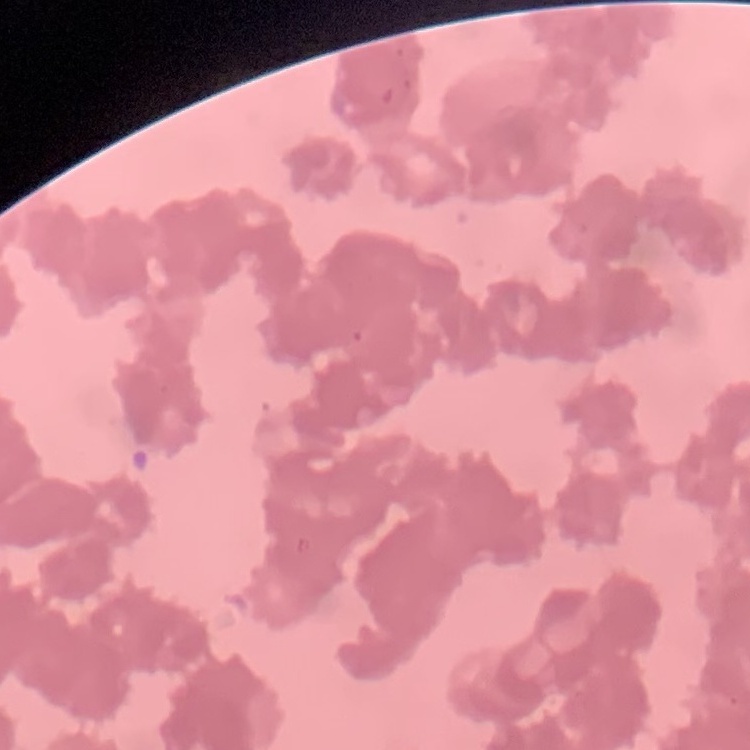
The red blood cells show rouleaux formation. One tile cut from a larger photomicrograph. Thin blood film. Stained with either Field's or Giemsa.